Locate every leukocyte (white blood cell).
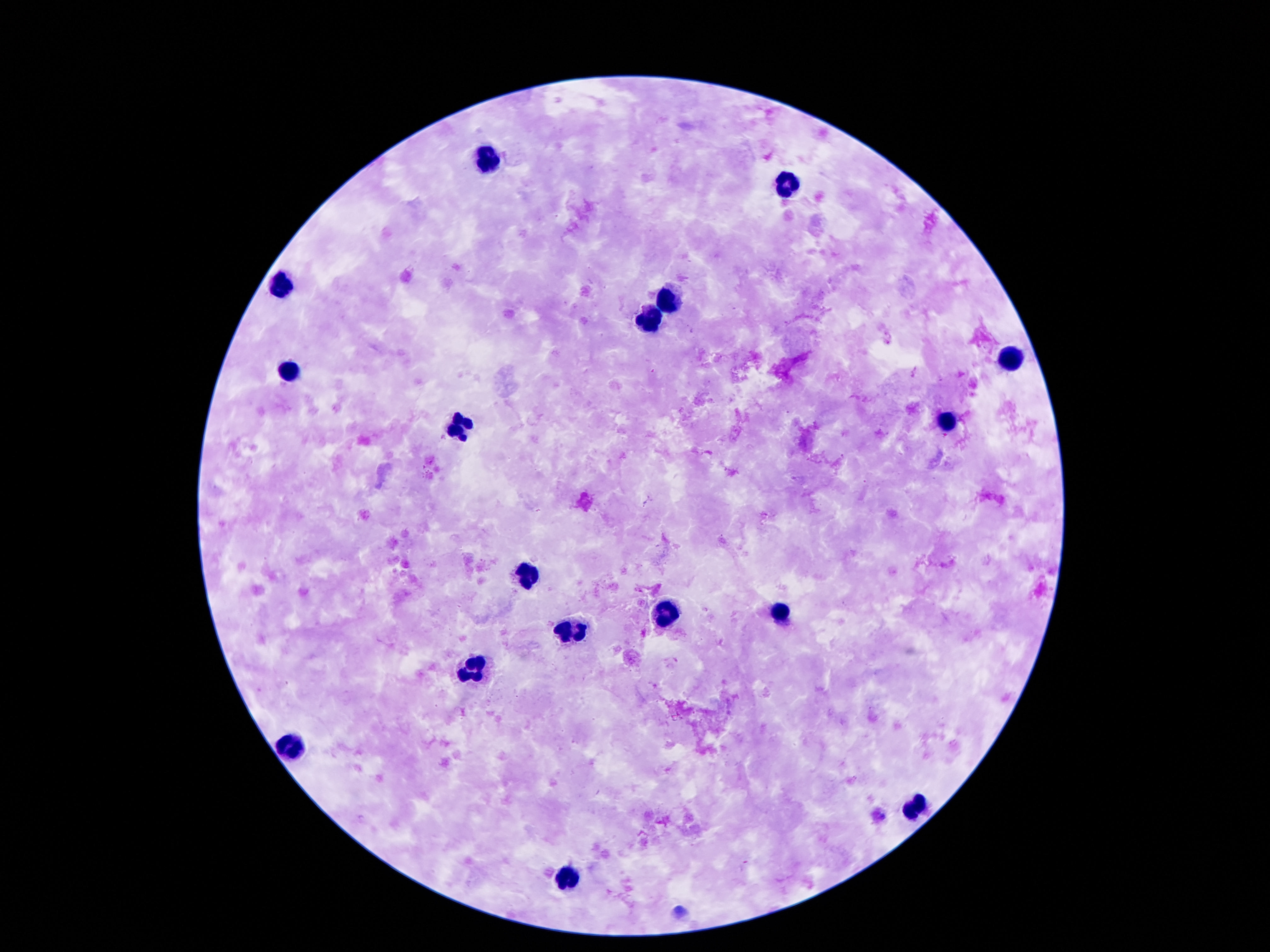
Approximate centers as {x, y} in pixels.
Leukocytes: {487, 160}, {783, 185}, {283, 286}, {667, 299}, {649, 318}, {1006, 358}, {290, 373}, {943, 424}, {455, 425}, {525, 577}, {665, 614}, {777, 615}, {567, 635}, {472, 671}, {290, 751}, {913, 807}, {565, 879}.

image size = 1270×952 pixels
stain = Giemsa
preparation = thick peripheral-blood smear
patient malaria status = uninfected
capture = smartphone camera through the microscope eyepiece
magnification = 100x
field of view = single